Give the preparation type.
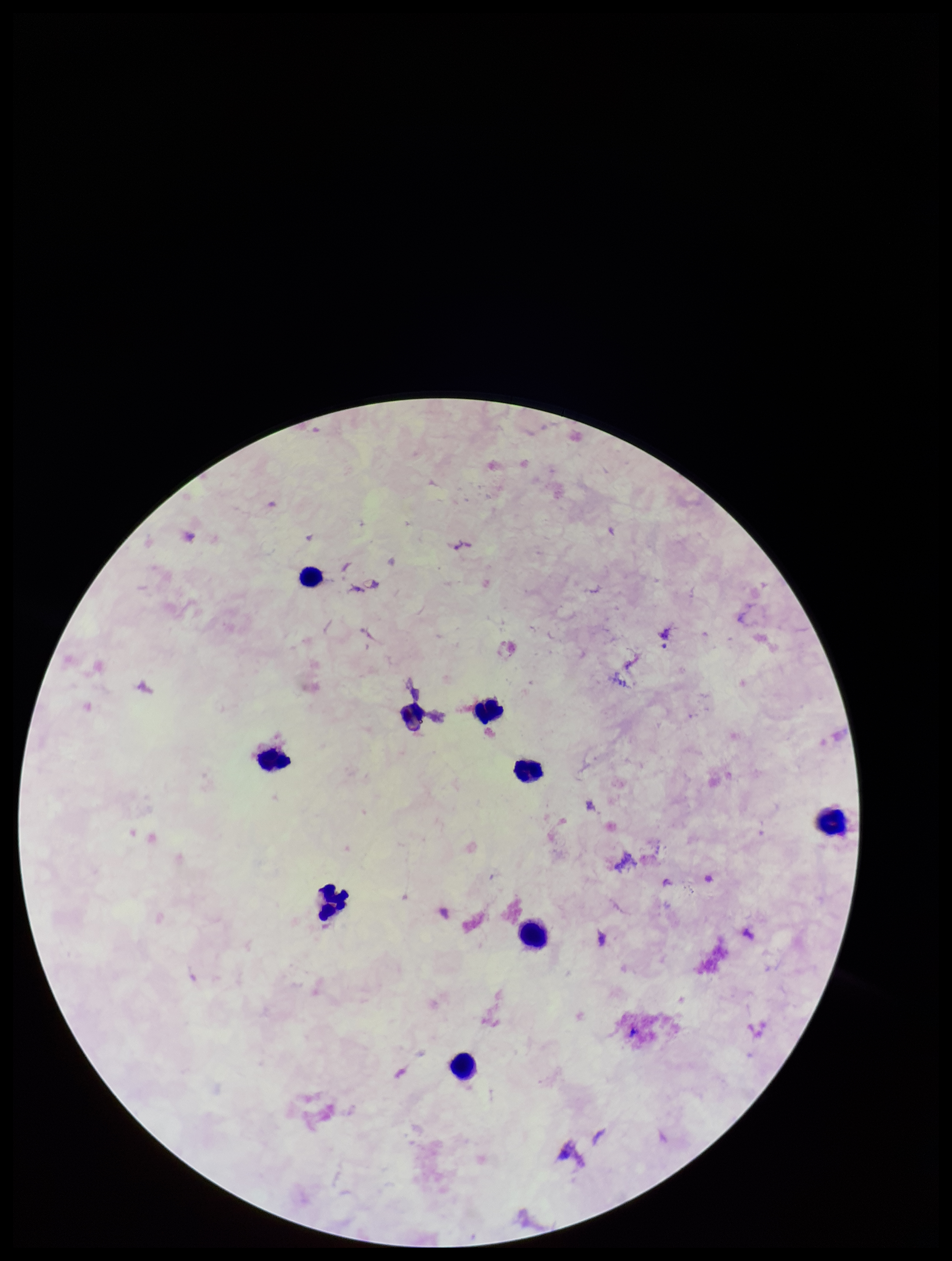
Thick.

Summary:
  - Field of view: single
  - Patient malaria status: negative
  - Capture: smartphone photograph through the microscope eyepiece
  - Stain: Giemsa
  - Parasite count: 0
  - Plasmodium parasites: none seen
  - Leukocyte count: 9
  - Image size: 952×1261 pixels